State which parasite is depicted.
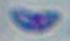

This is Toxoplasma gondii.

modality = micrograph
magnification = 1000x